Give the position of every Plasmodium parasite visible.
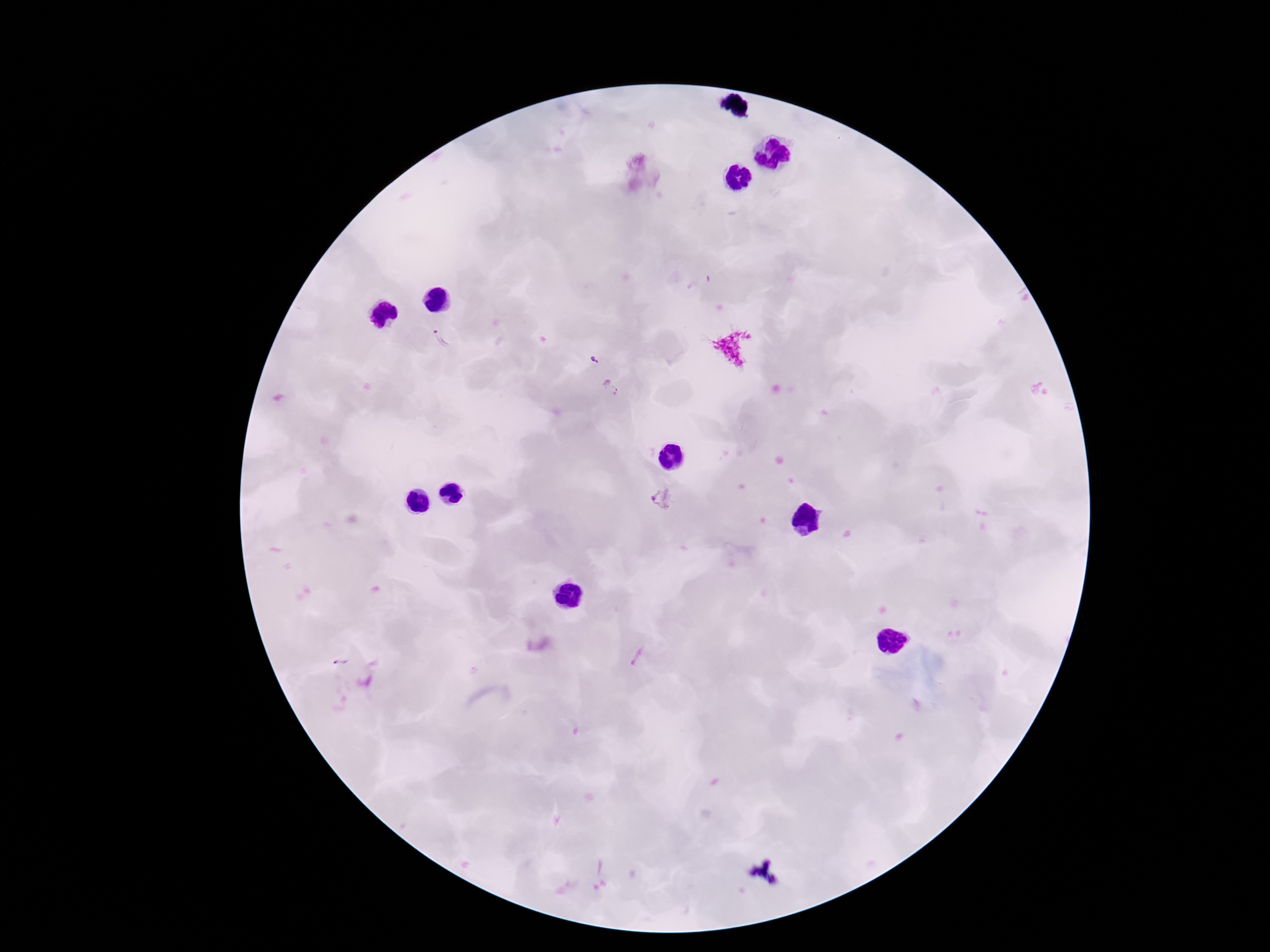

Approximate object centers, in pixels from the top-left corner.
Plasmodium parasites: (x=699, y=282), (x=440, y=339), (x=594, y=358), (x=611, y=388), (x=663, y=498), (x=637, y=657), (x=339, y=660).

100x magnification. Giemsa stain. Patient malaria status: infected. Photographed through the microscope eyepiece with a smartphone camera. Image is 1270×952 pixels. Thick peripheral-blood smear. Single field of view.